Identify the parasite.
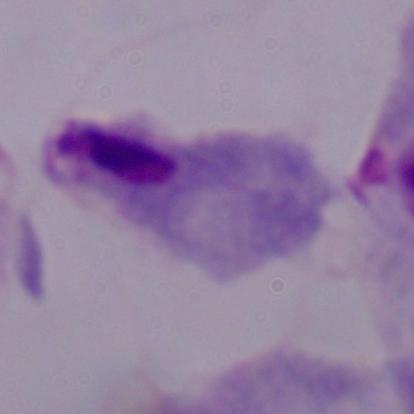
A trichomonad.

modality = micrograph
magnification = 1000x